Give the extent of all Plasmodium malariae-infected red blood cells.
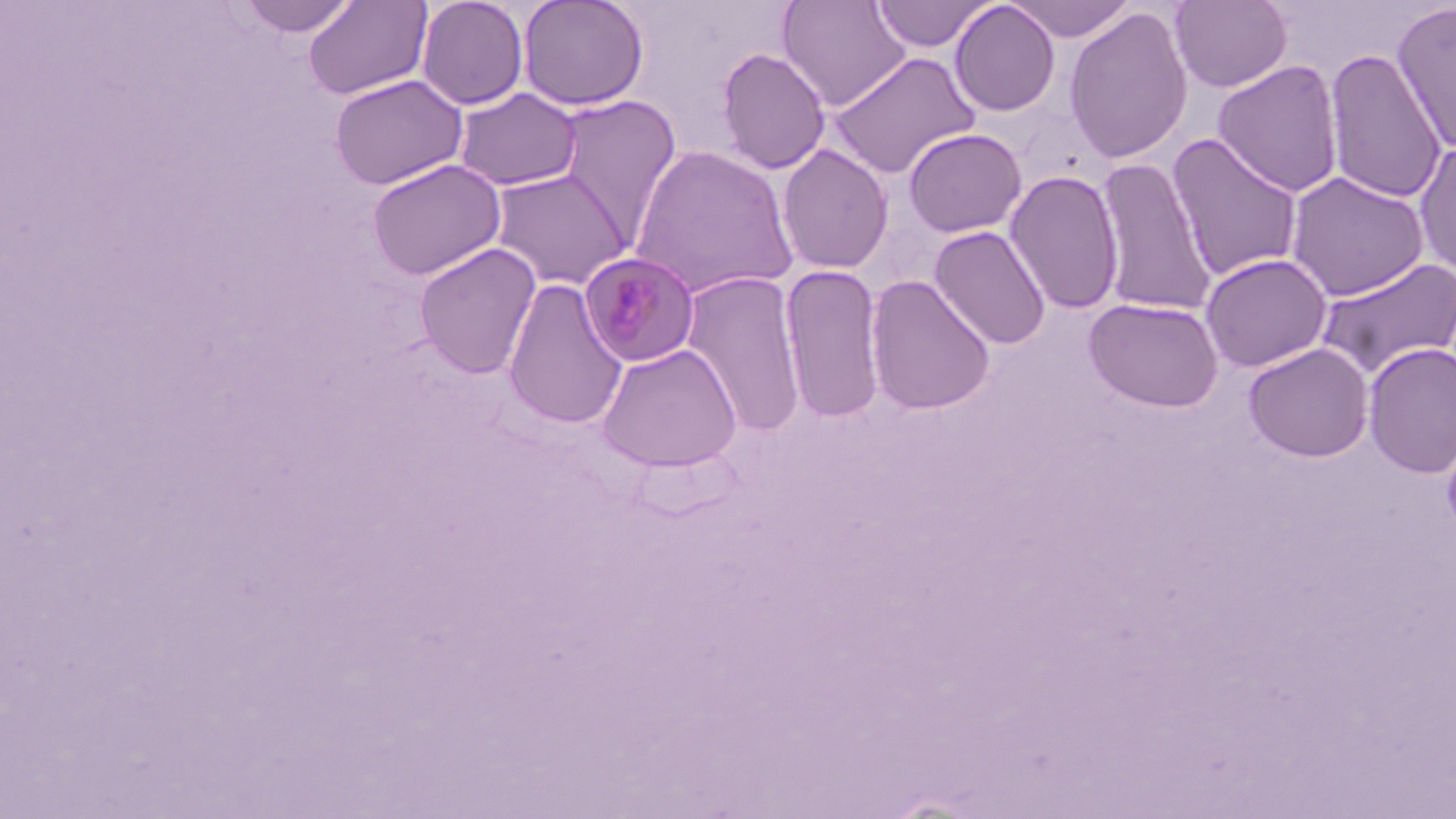
Approximate bounding boxes as [x1, y1, x2, y2] in pixels.
Plasmodium malariae-infected red blood cells: [578, 252, 701, 369].

Summary:
  - Uninfected red blood cell locations: [237, 0, 360, 38], [303, 0, 433, 101], [416, 0, 529, 110], [517, 0, 649, 111], [776, 0, 911, 111], [870, 0, 998, 53], [1006, 0, 1138, 42], [1169, 0, 1293, 92], [1391, 0, 1456, 154], [948, 1, 1062, 117], [1063, 8, 1194, 165], [716, 48, 830, 175], [1323, 48, 1447, 204], [826, 51, 982, 178], [1212, 60, 1344, 197], [329, 73, 468, 190], [453, 87, 583, 192], [553, 94, 682, 243], [902, 128, 1027, 238], [1166, 132, 1304, 283], [1413, 141, 1456, 280], [776, 143, 894, 275], [628, 144, 799, 300], [1093, 157, 1217, 317], [366, 158, 506, 281], [490, 169, 633, 290], [1004, 169, 1125, 315], [1285, 171, 1430, 301], [928, 225, 1052, 350], [413, 242, 542, 379], [1199, 253, 1332, 373], [1314, 256, 1456, 380], [779, 264, 887, 424], [680, 271, 807, 437], [865, 274, 996, 416], [501, 278, 628, 429], [1083, 297, 1224, 413], [1242, 342, 1375, 463], [596, 343, 742, 472], [1362, 343, 1456, 479], [1440, 419, 1456, 540]
  - Slide-level diagnosis: Plasmodium malariae
  - Field of view: single
  - Modality: light microscopy
  - Magnification: 1000x
  - Preparation: thin blood film
  - Stain: May-Grünwald-Giemsa
  - Image size: 1456×819 pixels